Assess this cell for malaria.
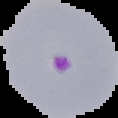

It is parasitized.

From a thin blood smear. Cell region segmented out of the field of view; the surrounding area is masked to black. Image is 118×118 pixels.